Assess this cell for malaria.
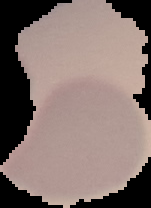

Uninfected.

From a thin blood film. Cell region segmented out of the field of view; the surrounding area is masked to black. Image is 151×208 pixels.